Assess this cell for malaria.
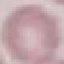

It is uninfected.

capture: smartphone through the microscope eyepiece
image_type: automatically extracted cell patch, resized to 64 × 64 pixels
stain: Giemsa
preparation: thin smear